Locate every malaria parasite.
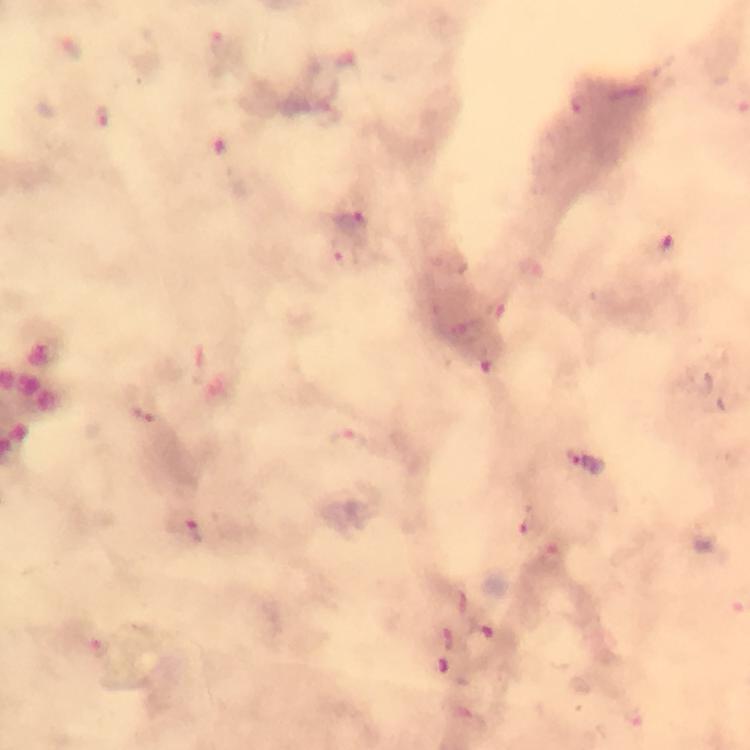

Approximate centers as [x, y] in pixels.
Malaria parasites: [70, 45], [586, 106], [106, 122], [353, 226], [348, 260], [350, 443], [585, 461], [531, 525], [186, 526], [485, 636], [448, 637], [99, 650], [445, 668].

magnification = 100x
stain = Giemsa
capture = smartphone mounted on the microscope
context = from a diagnostic examination for malaria
immersion oil = applied
image size = 750×750 pixels
cropped from = one field of view
preparation = thick blood smear